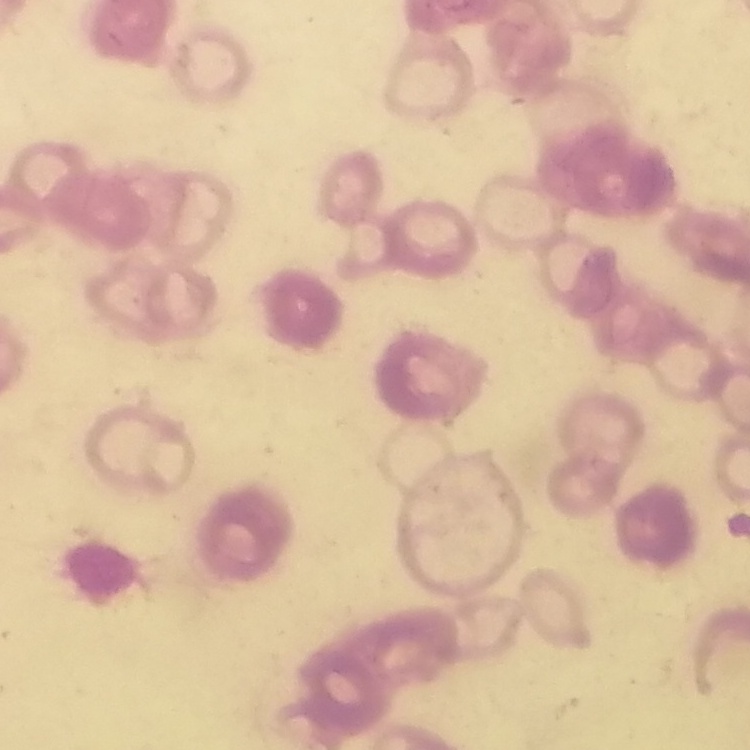
Summary:
  - Red blood cell morphology: rouleaux formation
  - Image type: square crop of a larger photomicrograph
  - Preparation: thin blood smear
  - Stain: Field's or Giemsa